Give the position of every Plasmodium parasite.
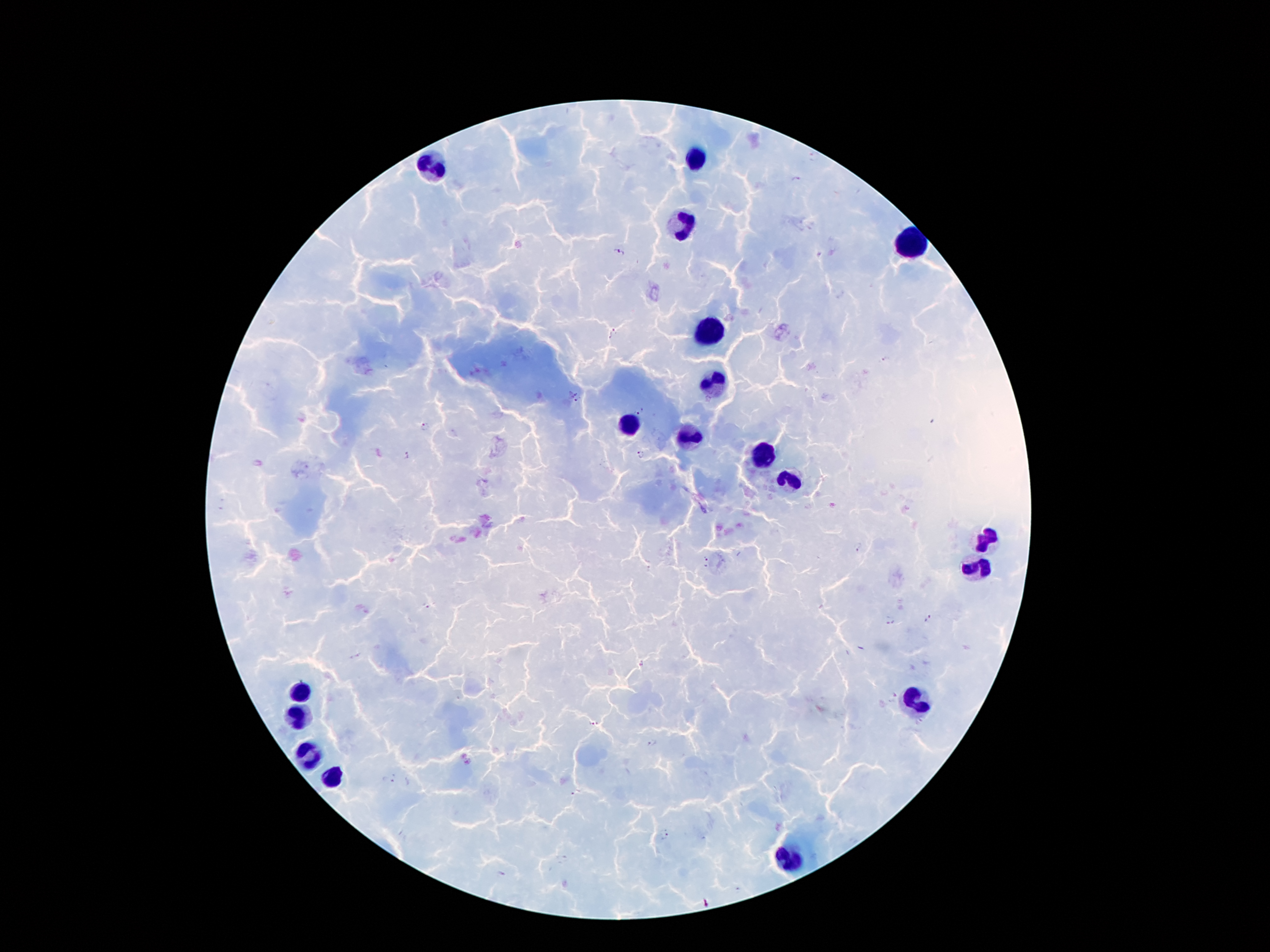
Approximate centers as (x, y) in pixels.
Plasmodium parasites: (796, 179), (618, 253), (615, 331), (610, 337), (886, 360), (576, 397), (640, 414), (425, 427), (641, 453), (406, 456), (858, 545), (707, 558), (706, 568), (425, 605), (929, 619), (890, 623), (641, 664), (893, 696), (592, 725), (652, 742), (388, 780), (577, 794), (665, 834).

Leukocyte locations: (699, 160), (437, 165), (683, 226), (908, 244), (711, 333), (713, 384), (627, 423), (689, 435), (760, 458), (789, 480), (986, 537), (978, 566), (299, 691), (916, 703), (299, 712), (307, 757), (332, 777), (787, 859). Giemsa stain. One field from this slide. 100x magnification. Photographed through the microscope eyepiece with a smartphone camera. Image is 1270×952 pixels. Thick blood smear. Patient malaria status: infected with Plasmodium falciparum.